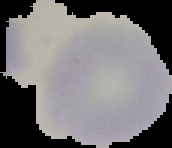

Summary:
  - Preparation: thin blood smear
  - Image type: cell region segmented out of the field of view; surrounding area masked to black
  - Malaria status: uninfected
  - Image size: 172×148 pixels